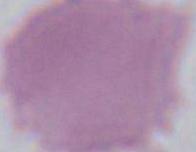
Summary:
  - Magnification: 1000x
  - Identification: red blood cell
  - Modality: photomicrograph